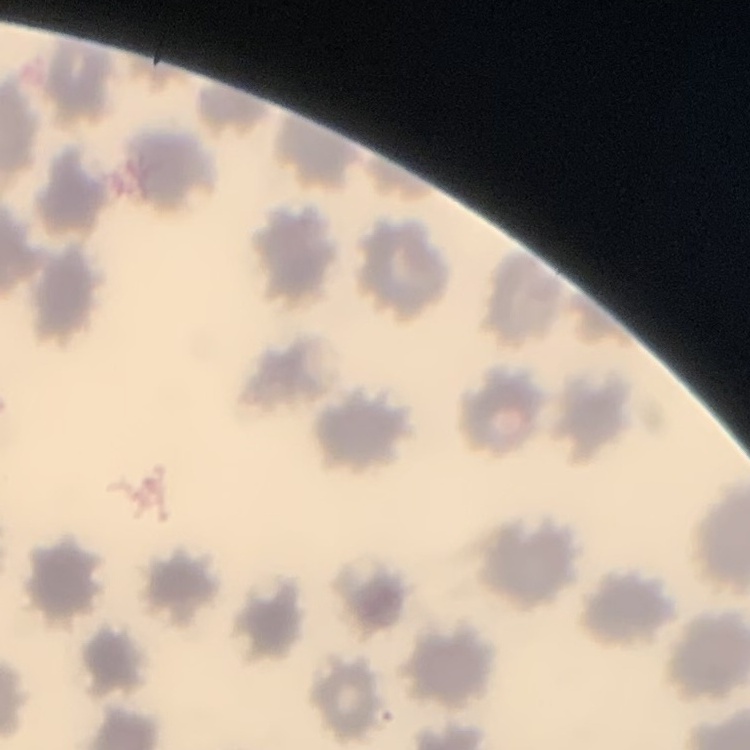

{
  "erythrocyte_morphology": "no rouleaux formation",
  "image_type": "one tile cut from a larger photomicrograph",
  "preparation": "thin blood film",
  "stain": "Field's or Giemsa"
}